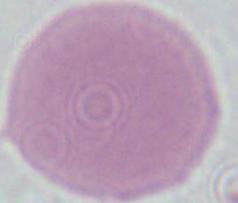 1000x magnification. A red blood cell is seen. Photomicrograph.